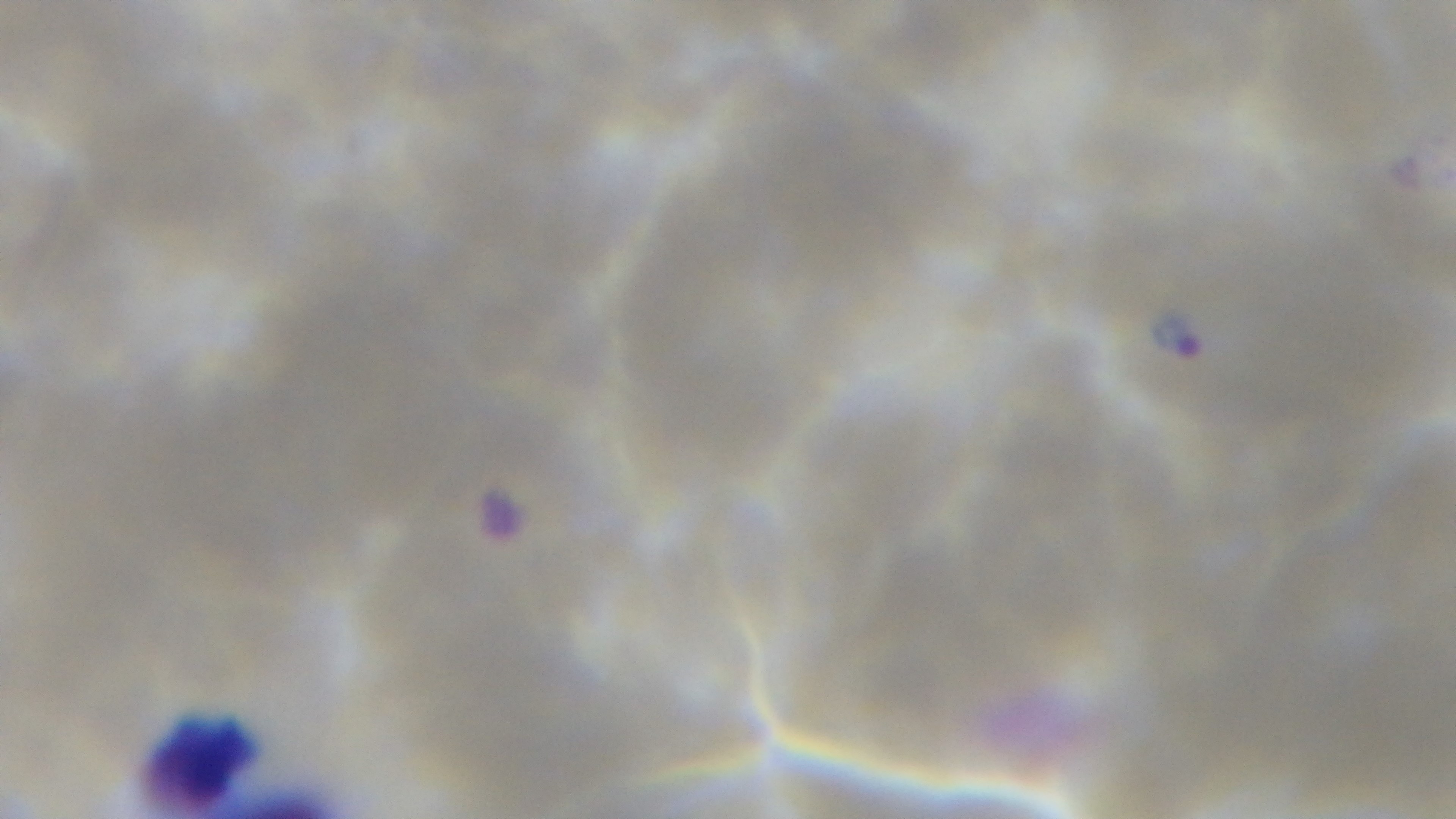

stain = Giemsa
field of view = one from the slide
malaria status = infected
objective = 100x oil immersion
preparation = thin
capture = mounted 4K digital camera
modality = light microscopy